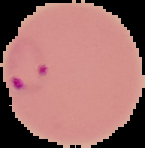
Segmented cell region on a black background. Result: Plasmodium parasites identified. Image is 145×148 pixels. From a thin blood smear.